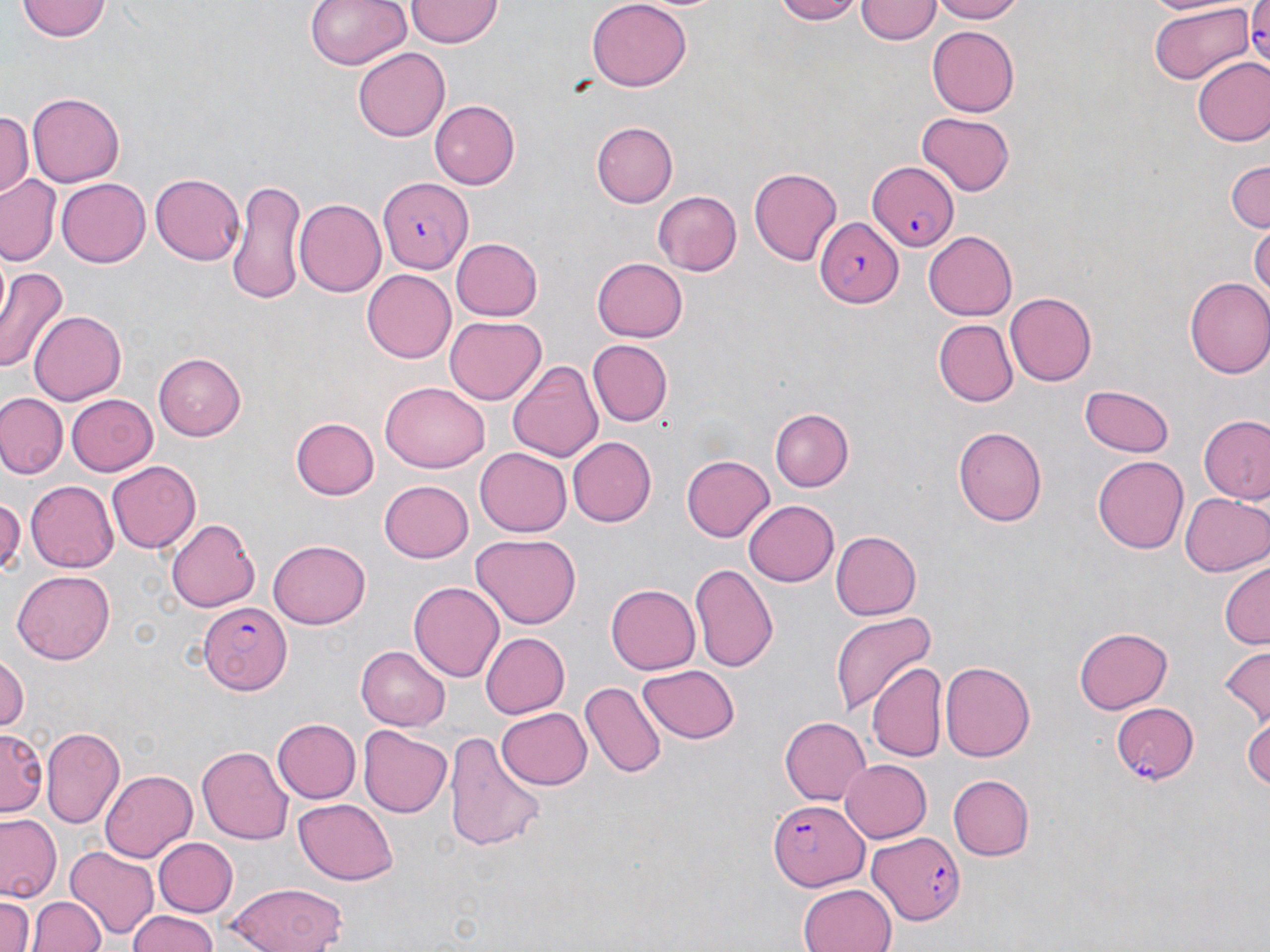
slide-level diagnosis = Plasmodium falciparum
stain = May-Grünwald-Giemsa
image size = 1270×952 pixels
magnification = 1000x
preparation = thin blood film
field of view = single
modality = light microscopy
uninfected red blood cell locations = approximate bounding boxes as [x1, y1, x2, y2] in pixels: [19, 0, 110, 42], [304, 0, 411, 73], [769, 0, 868, 24], [927, 0, 1031, 23], [406, 1, 502, 47], [586, 1, 692, 92], [856, 1, 940, 46], [1148, 5, 1253, 83], [927, 28, 1020, 115], [355, 46, 450, 138], [1191, 56, 1270, 145], [26, 93, 124, 187], [430, 100, 521, 189], [0, 108, 33, 203], [917, 111, 1016, 196], [591, 122, 678, 208], [1226, 160, 1270, 235], [747, 167, 843, 266], [150, 173, 245, 267], [1, 174, 62, 265], [56, 177, 149, 267], [226, 178, 307, 303], [653, 190, 743, 274], [294, 200, 385, 297], [1250, 222, 1270, 305], [924, 230, 1020, 319], [453, 236, 544, 320], [592, 257, 687, 343], [0, 263, 69, 377], [361, 270, 455, 363], [1184, 276, 1270, 380], [1004, 293, 1097, 386], [30, 308, 126, 406], [445, 316, 546, 405], [933, 318, 1018, 404], [586, 340, 671, 426], [153, 352, 244, 440], [507, 362, 604, 461], [382, 379, 488, 470], [1080, 385, 1175, 457], [63, 392, 157, 477], [0, 393, 66, 480], [771, 409, 855, 491], [1197, 414, 1270, 506], [289, 416, 382, 500], [954, 427, 1048, 526], [568, 436, 655, 527], [474, 449, 571, 536], [680, 454, 774, 540], [1091, 455, 1188, 553], [106, 458, 200, 550], [24, 480, 117, 571], [378, 480, 472, 564], [1180, 492, 1269, 576], [0, 494, 25, 580], [743, 499, 839, 586], [167, 518, 259, 613], [831, 531, 923, 619], [472, 534, 581, 627], [267, 540, 371, 630], [1219, 559, 1269, 651], [691, 563, 779, 671], [11, 570, 117, 664], [409, 581, 503, 683], [606, 583, 702, 673], [830, 610, 934, 716], [1074, 628, 1172, 713], [482, 631, 570, 719], [358, 644, 452, 727], [1216, 645, 1270, 729], [0, 652, 26, 739], [940, 659, 1036, 763], [870, 660, 945, 762], [640, 665, 739, 743], [580, 682, 666, 780], [498, 705, 593, 789], [1245, 713, 1270, 792], [779, 716, 871, 805], [272, 718, 361, 804], [41, 725, 124, 829], [356, 725, 452, 819], [3, 728, 44, 813], [446, 733, 545, 855], [198, 745, 293, 845], [839, 759, 931, 842], [100, 768, 197, 861], [949, 772, 1035, 861], [293, 794, 397, 883], [1, 814, 63, 900], [154, 837, 238, 917], [64, 845, 160, 938], [224, 881, 349, 952], [797, 884, 896, 952], [31, 895, 105, 952], [0, 897, 35, 952], [126, 910, 221, 952]
Plasmodium falciparum-infected red blood cell locations = approximate bounding boxes as [x1, y1, x2, y2] in pixels: [1247, 1, 1269, 79], [866, 160, 958, 251], [378, 177, 475, 272], [819, 216, 903, 305], [199, 603, 291, 693], [1110, 701, 1198, 782], [768, 800, 867, 886], [868, 831, 967, 925]